Identify the cell.
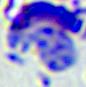
A leukocyte.

Summary:
  - Modality: photomicrograph
  - Magnification: 400x